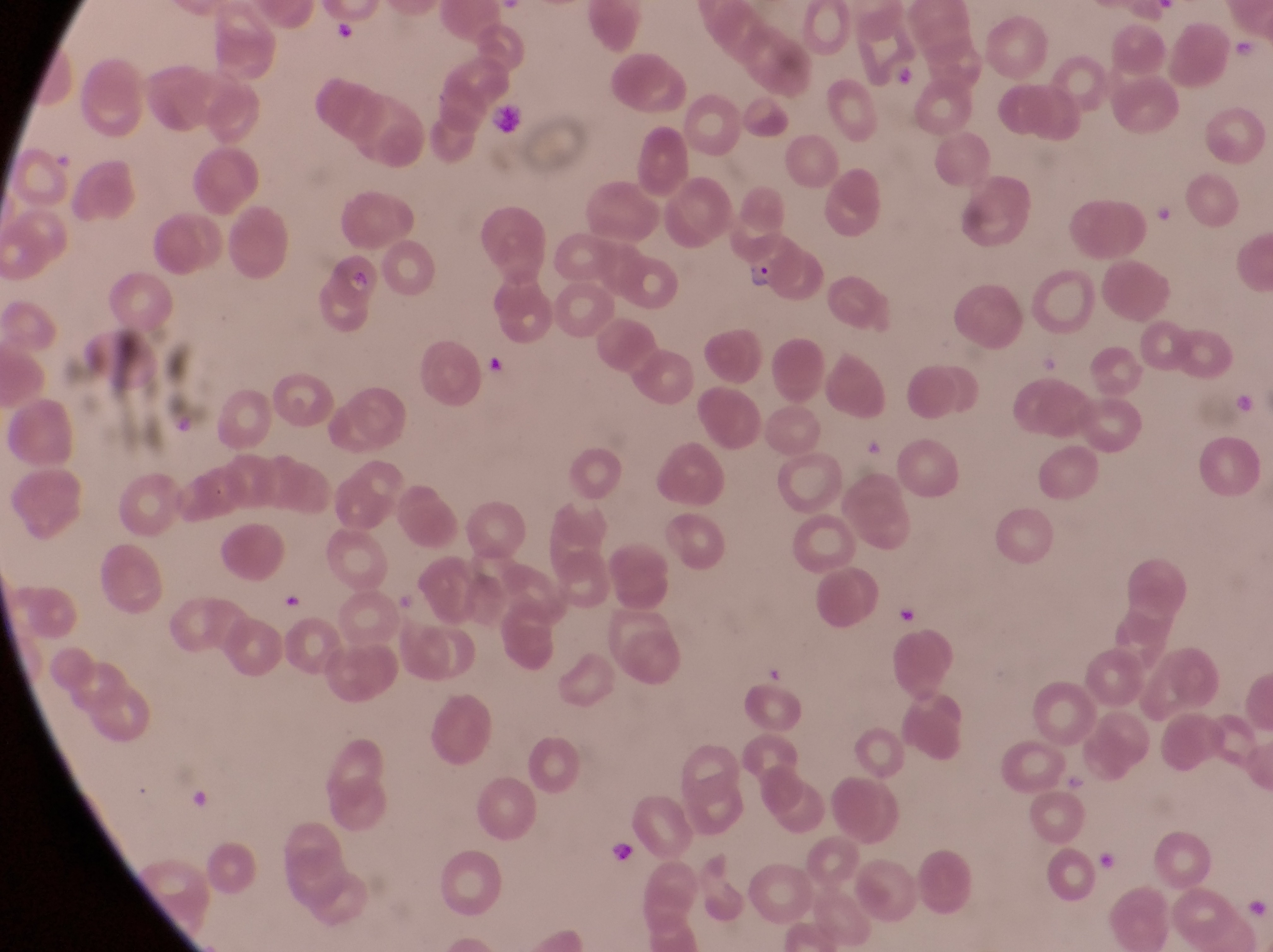

Approximate bounding boxes as left top right bottom in pixels.
Summary:
  - Trophozoite locations: 606 834 641 876
  - Artifact (platelet-like body, stain precipitate, or debris) locations: 486 104 528 144; 482 348 512 387
  - Parasitised red blood cell locations: 743 232 806 302
  - Capture: smartphone photograph through the eyepiece of an Olympus CX-23 microscope
  - Country: Uganda
  - Preparation: thin blood film
  - Field of view: single
  - Magnification: 1000x
  - Image size: 1273×952 pixels